Locate and identify every blood parasite.
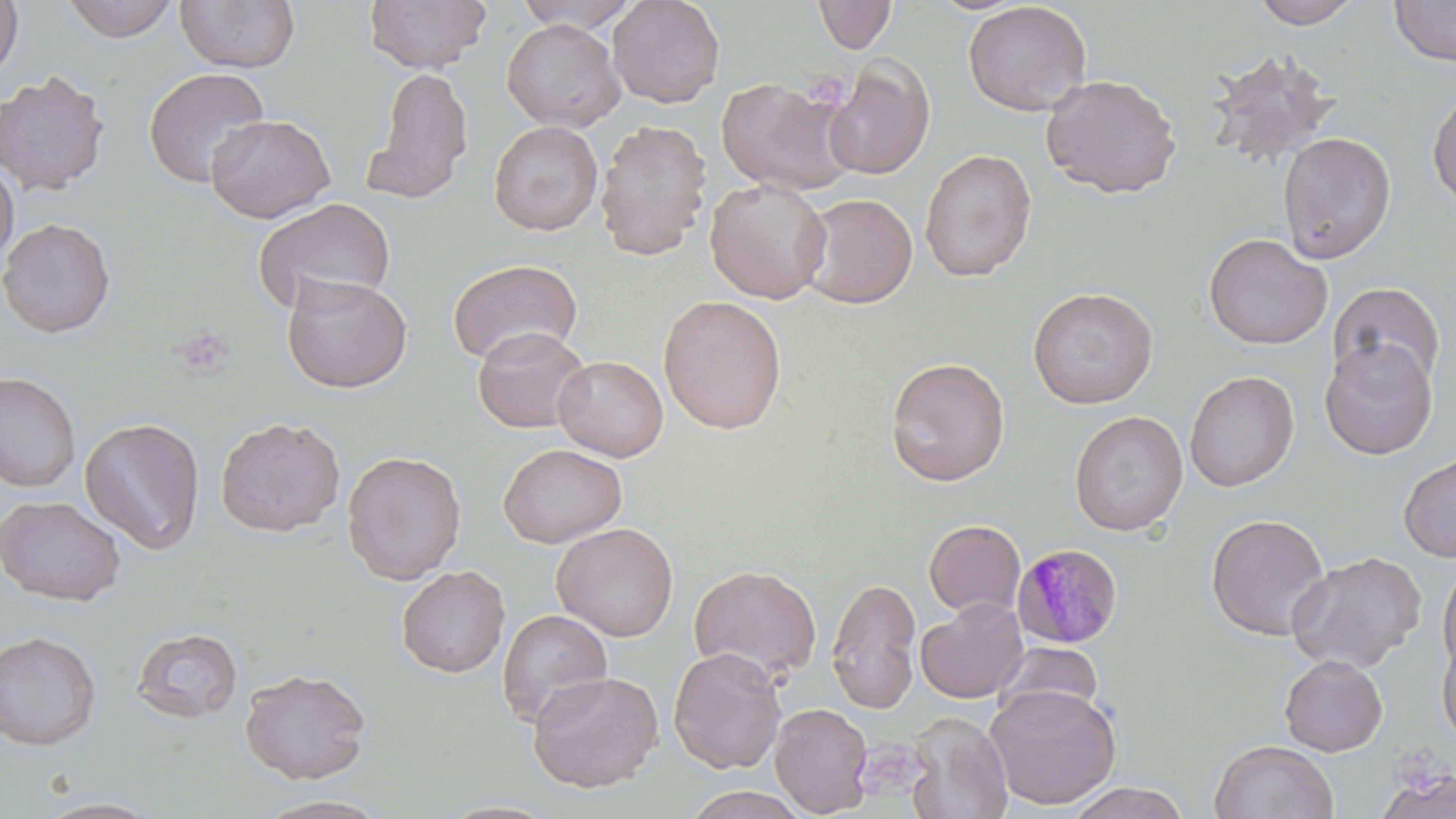
Approximate bounding boxes as (x1,y1)-(x2,y2) corner pairs in pixels.
Plasmodium malariae-infected red blood cells: (1011,543)-(1124,648).
No Plasmodium falciparum, Plasmodium ovale, Plasmodium vivax, Babesia divergens, or Trypanosoma brucei observed.

Summary:
  - Uninfected red blood cell locations: (0,0)-(24,84), (60,0)-(181,43), (363,0)-(490,73), (513,0)-(644,33), (607,0)-(726,108), (1249,0)-(1365,29), (1389,0)-(1456,66), (175,1)-(301,73), (813,1)-(898,54), (963,1)-(1092,117), (502,18)-(626,134), (1202,48)-(1342,174), (823,57)-(935,180), (366,66)-(474,201), (143,67)-(270,189), (0,70)-(111,197), (1040,73)-(1182,199), (716,76)-(858,196), (1427,86)-(1456,211), (205,114)-(335,223), (594,119)-(713,262), (488,120)-(603,236), (1277,132)-(1396,265), (919,148)-(1037,282), (0,159)-(19,267), (705,178)-(832,305), (798,192)-(919,309), (253,198)-(396,314), (0,217)-(116,338), (1202,232)-(1333,350), (446,258)-(582,366), (281,273)-(412,394), (1327,281)-(1445,389), (1027,286)-(1159,409), (658,295)-(788,434), (471,326)-(592,433), (1319,338)-(1438,460), (553,355)-(668,462), (885,356)-(1010,487), (1184,370)-(1299,492), (0,371)-(81,493), (1069,410)-(1188,536), (215,415)-(346,537), (79,417)-(206,555), (498,443)-(627,549), (341,449)-(467,584), (1398,451)-(1456,562), (0,494)-(128,606), (1205,512)-(1331,641), (923,519)-(1026,618), (551,522)-(679,641), (1286,550)-(1426,673), (1437,559)-(1456,676), (688,564)-(822,682), (396,565)-(511,678), (826,576)-(922,715), (915,599)-(1028,704), (496,608)-(613,728), (131,627)-(244,723), (0,630)-(102,749), (1436,635)-(1456,749), (992,641)-(1104,724), (668,646)-(787,775), (1279,654)-(1388,756), (239,667)-(372,783), (527,670)-(664,793), (985,683)-(1122,810), (769,702)-(874,818), (904,711)-(1013,819), (1208,740)-(1340,819), (1375,767)-(1456,819), (1064,781)-(1191,819), (680,786)-(811,819), (251,794)-(394,818)
  - Slide-level diagnosis: Plasmodium malariae
  - Modality: light microscopy
  - Stain: May-Grünwald-Giemsa
  - Magnification: 1000x
  - Image size: 1456×819 pixels
  - Field of view: single
  - Preparation: thin blood smear